Locate the red blood cells and classify each one as Plasmodium falciparum-infected, uninfected, or of indeterminate infection status.
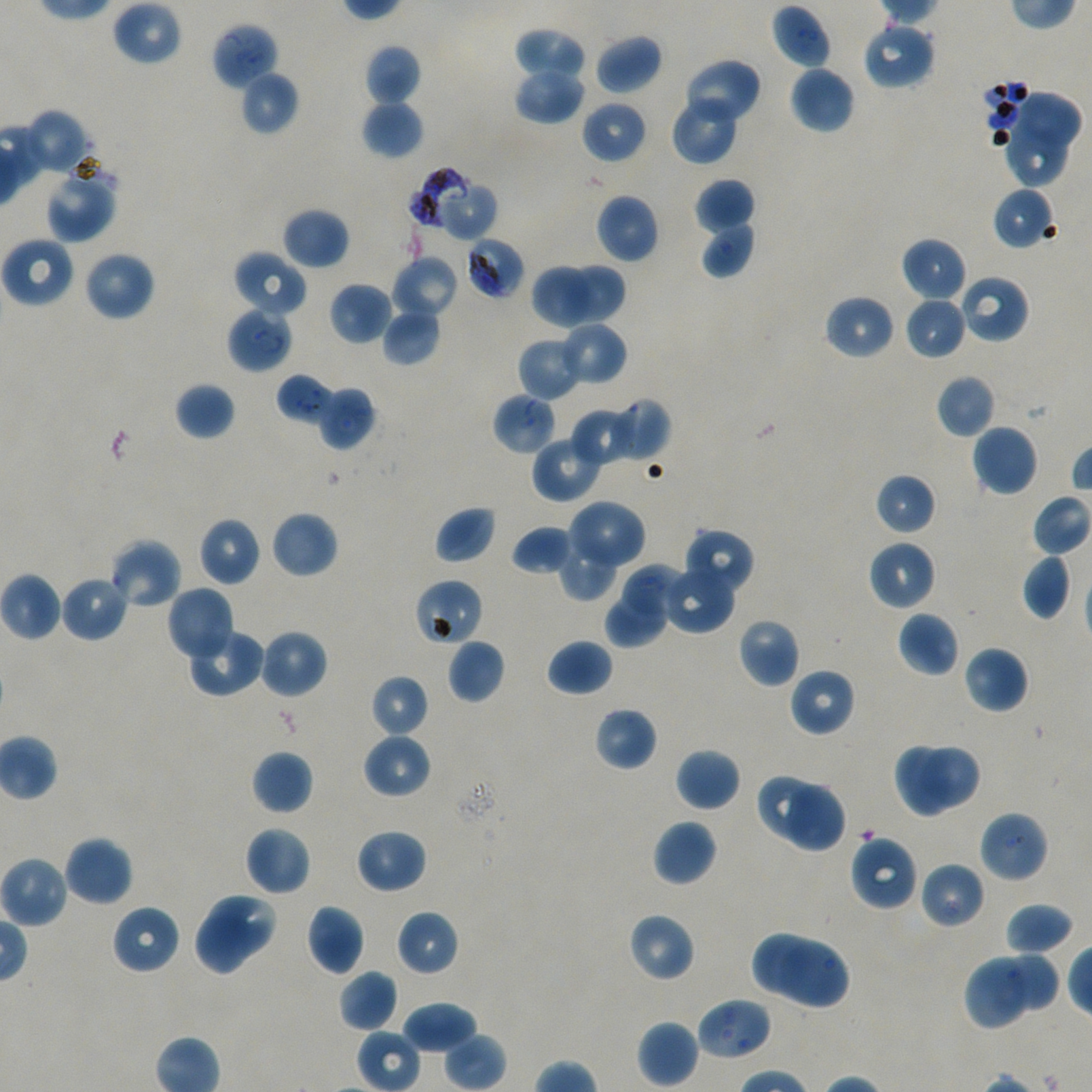
Approximate bounding boxes as {x1, y1, x2, y2} in pixels. Not every red blood cell is marked. A life-cycle stage — or a range of stages, where the recorded stages span more than one — follows each staged infected red blood cell.
Infected red blood cells: {226, 307, 293, 374} late ring to early trophozoite; {276, 374, 334, 426} late ring to early trophozoite.
Red blood cells of indeterminate infection status: {410, 168, 497, 243}, {466, 236, 525, 299}, {958, 273, 1031, 344}, {413, 579, 484, 647}.
Uninfected red blood cells: {111, 0, 182, 67}, {770, 5, 832, 70}, {211, 21, 279, 91}, {861, 21, 935, 90}, {513, 27, 585, 84}, {596, 33, 663, 94}, {364, 44, 421, 106}, {682, 57, 762, 127}, {513, 65, 584, 124}, {789, 65, 855, 134}, {239, 69, 299, 136}, {1017, 90, 1084, 146}, {669, 95, 740, 166}, {361, 98, 424, 160}, {581, 100, 648, 164}, {24, 109, 90, 175}, {1001, 118, 1069, 189}, {44, 164, 117, 244}, {695, 177, 755, 234}, {991, 186, 1057, 250}, {595, 193, 659, 264}, {282, 207, 350, 269}, {699, 219, 756, 279}, {1, 235, 75, 308}, {901, 236, 967, 302}, {84, 250, 156, 322}, {233, 250, 309, 318}, {391, 255, 460, 321}, {533, 263, 621, 329}, {565, 263, 625, 325}, {533, 267, 586, 329}, {329, 282, 394, 346}, {823, 294, 895, 361}, {905, 297, 967, 359}, {382, 306, 442, 367}, {558, 322, 627, 386}, {517, 337, 583, 401}, {935, 374, 996, 439}, {175, 381, 236, 441}, {316, 385, 376, 450}, {492, 392, 557, 454}, {605, 399, 669, 463}, {571, 406, 639, 468}, {971, 424, 1038, 497}, {531, 433, 604, 503}, {874, 473, 936, 535}, {1032, 493, 1091, 558}, {566, 500, 646, 577}, {435, 505, 497, 564}, {270, 511, 338, 579}, {198, 516, 262, 586}, {512, 525, 574, 575}, {683, 528, 755, 598}, {108, 537, 183, 611}, {867, 540, 936, 611}, {557, 541, 618, 600}, {1021, 553, 1072, 619}, {662, 563, 735, 635}, {624, 564, 679, 619}, {0, 571, 62, 641}, {60, 575, 129, 642}, {165, 585, 235, 664}, {605, 592, 667, 647}, {896, 611, 960, 677}, {738, 619, 800, 689}, {185, 626, 266, 698}, {259, 629, 328, 699}, {447, 638, 506, 705}, {546, 638, 613, 696}, {962, 644, 1030, 714}, {788, 667, 856, 737}, {370, 674, 429, 737}, {593, 706, 658, 771}, {361, 732, 432, 799}, {893, 743, 949, 818}, {922, 747, 979, 807}, {675, 748, 741, 812}, {251, 750, 313, 815}, {755, 772, 824, 841}, {786, 782, 848, 854}, {978, 809, 1049, 884}, {653, 819, 718, 887}, {243, 826, 312, 896}, {354, 829, 428, 894}, {848, 833, 920, 913}, {63, 835, 134, 906}, {0, 853, 69, 930}, {920, 861, 985, 930}, {208, 892, 274, 960}, {1004, 903, 1075, 956}, {111, 904, 181, 975}, {306, 904, 365, 975}, {395, 909, 460, 977}, {193, 913, 253, 977}, {627, 913, 695, 982}, {752, 932, 814, 994}, {777, 941, 850, 1011}, {1000, 947, 1060, 1011}, {965, 953, 1029, 1029}, {338, 970, 399, 1034}, {695, 996, 772, 1061}, {401, 999, 477, 1054}, {636, 1019, 699, 1088}, {444, 1034, 507, 1091}.

Summary:
  - Culture: in-vitro Plasmodium falciparum strain NF54, static
  - Field of view: one from this slide
  - Stain: Giemsa
  - Preparation: thin blood film
  - Image size: 1092×1092 pixels
  - Donor blood group: A+/O+
  - Objective: 100x, oil immersion, numerical aperture 1.45